Assess this cell for malaria.
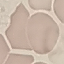
Uninfected.

Summary:
  - Preparation: thin smear
  - Image type: cell patch, automatically extracted from a larger field of view and resized to 64 × 64 pixels
  - Stain: Giemsa
  - Capture: smartphone camera at the microscope eyepiece